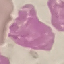
malaria status = uninfected
image type = cell patch, automatically extracted from a larger field of view and resized to 64 × 64 pixels
stain = Giemsa
capture = smartphone camera at the microscope eyepiece
preparation = thin smear